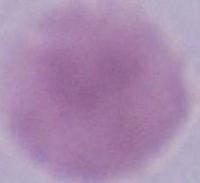

Summary:
  - Identification: erythrocyte
  - Magnification: 1000x
  - Modality: micrograph